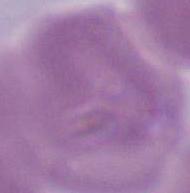

1000x magnification. A red blood cell is seen. Micrograph.